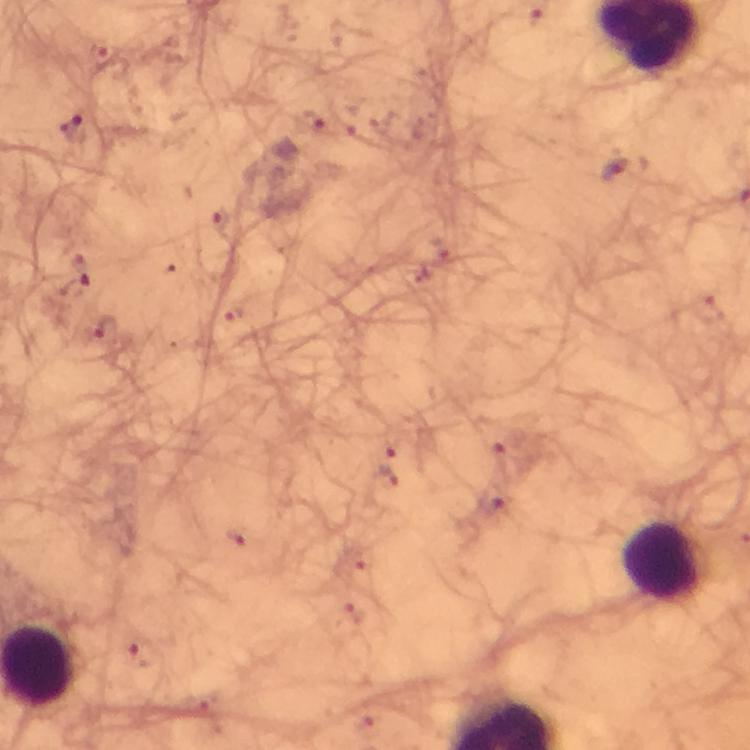

Approximate centers as [x, y] in pixels. Plasmodium parasite locations: [72, 128], [623, 169], [385, 477]. Leukocyte locations: [664, 563]. From a diagnostic examination for malaria. Thick blood film. Immersion oil was used. Image is 750×750 pixels. Smartphone photograph taken through a microscope. At 100x magnification. A crop from one field of view. Giemsa stain.